Identify the preparation type.
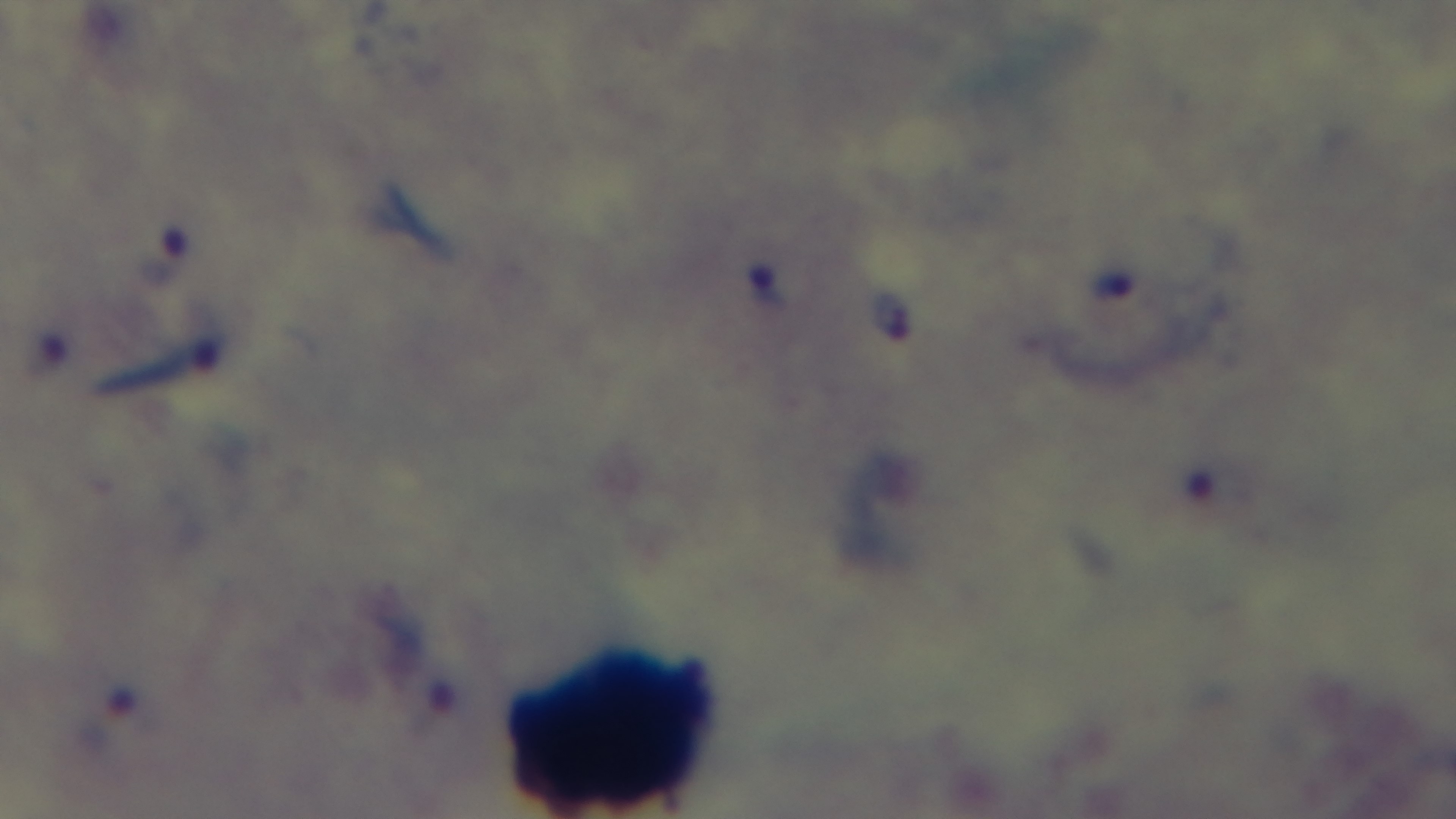
Thick.

Mounted 4K digital camera. Single field of view. Photomicrograph. Giemsa-stained. Oil-immersion objective, 100x. Malaria status: positive.